Name the parasite shown.
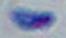

This is Toxoplasma gondii.

Photomicrograph. 1000x magnification.